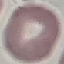

malaria status = uninfected
stain = Giemsa
capture = smartphone through the microscope eyepiece
preparation = thin blood film
image type = cell patch, automatically extracted from a larger field of view and resized to 64 × 64 pixels